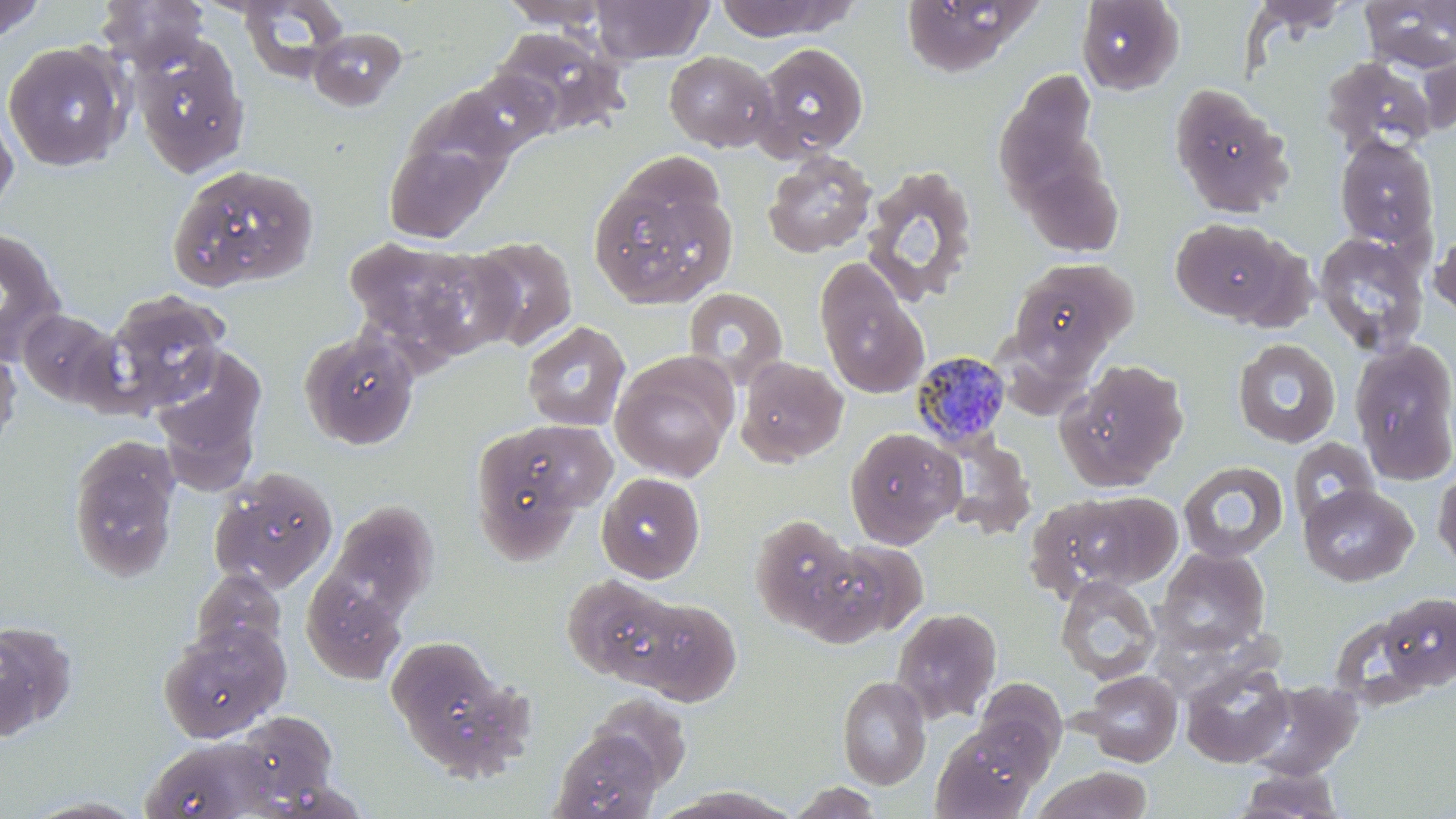

Plasmodium malariae-infected red blood cell locations = approximate bounding boxes as (x1, y1, x2, y2) in pixels: (911, 349, 1012, 450)
slide-level diagnosis = Plasmodium malariae
modality = light microscopy
magnification = 1000x
preparation = thin blood film
field of view = one of a larger specimen
image size = 1456×819 pixels
uninfected red blood cell locations = approximate bounding boxes as (x1, y1, x2, y2) in pixels: (97, 0, 209, 72), (237, 0, 349, 82), (591, 0, 713, 64), (899, 0, 1039, 77), (1076, 0, 1184, 96), (0, 1, 45, 44), (498, 1, 615, 30), (713, 1, 860, 41), (1248, 1, 1353, 36), (1359, 1, 1456, 73), (308, 26, 408, 111), (490, 27, 628, 139), (132, 36, 250, 179), (2, 41, 130, 171), (751, 42, 869, 162), (664, 50, 777, 152), (1320, 55, 1435, 156), (455, 70, 558, 157), (994, 71, 1104, 207), (1169, 83, 1293, 218), (0, 105, 19, 219), (1334, 133, 1440, 252), (383, 138, 497, 242), (762, 150, 879, 259), (1019, 161, 1125, 258), (860, 165, 980, 305), (173, 167, 316, 285), (588, 177, 735, 309), (1171, 216, 1290, 323), (1430, 220, 1455, 324), (0, 228, 65, 363), (1313, 232, 1429, 357), (344, 234, 514, 368), (467, 235, 578, 350), (813, 258, 929, 399), (1007, 258, 1138, 368), (682, 286, 789, 388), (104, 290, 230, 414), (17, 309, 123, 408), (522, 321, 631, 432), (299, 329, 420, 451), (1232, 338, 1341, 448), (1350, 338, 1456, 487), (149, 344, 268, 486), (0, 345, 22, 455), (610, 353, 737, 482), (735, 356, 848, 466), (1056, 359, 1189, 491), (469, 420, 610, 561), (844, 427, 964, 547), (937, 433, 1037, 540), (68, 435, 181, 583), (1288, 437, 1380, 528), (1178, 461, 1289, 564), (1432, 464, 1456, 572), (209, 467, 338, 594), (596, 472, 705, 582), (583, 474, 698, 685), (1298, 484, 1417, 586), (1073, 491, 1183, 587), (1025, 495, 1153, 601), (326, 499, 439, 620), (750, 513, 861, 634), (799, 540, 923, 645), (1155, 547, 1270, 655), (190, 568, 287, 663), (301, 575, 405, 683), (562, 575, 689, 688), (1055, 575, 1161, 685), (1376, 591, 1455, 693), (631, 598, 742, 706), (892, 607, 1002, 723), (0, 619, 78, 742), (158, 623, 290, 742), (386, 635, 515, 765), (1180, 662, 1294, 768), (1081, 670, 1182, 767), (837, 675, 931, 789), (974, 677, 1067, 771), (1246, 680, 1363, 780), (589, 692, 692, 789), (235, 710, 339, 809), (930, 726, 1042, 819), (549, 729, 663, 819), (140, 735, 282, 819), (1033, 767, 1152, 819), (1232, 767, 1349, 818), (786, 781, 886, 818), (652, 788, 800, 818), (18, 795, 152, 818)
stain = May-Grünwald-Giemsa